Assess this cell for malaria.
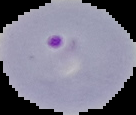

It is parasitized.

Image is 136×115 pixels. The area outside the segmented cell region is set to black. From a thin blood film.